Identify the parasite.
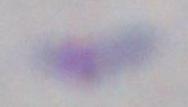
This is Toxoplasma gondii.

Micrograph. Captured at 1000x magnification.